Identify the cell.
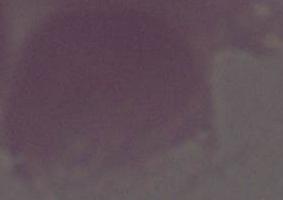

An erythrocyte.

modality: photomicrograph
magnification: 1000x